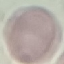
result: negative for malaria parasites
capture: smartphone through the microscope eyepiece
preparation: thin smear
image_type: automatically extracted cell patch, resized to 64 × 64 pixels
stain: Giemsa